Name the parasite shown.
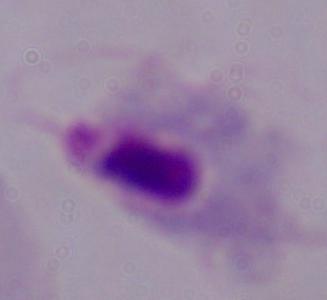

This is a trichomonad.

modality = micrograph
magnification = 1000x